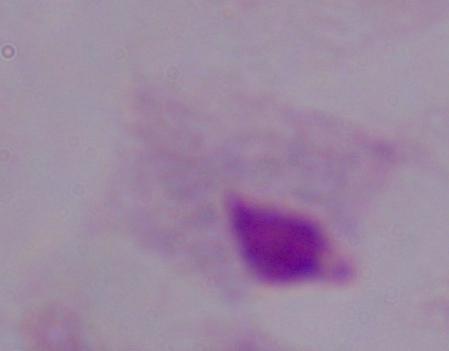
modality = photomicrograph
identification = trichomonad
magnification = 1000x